Classify this cell by malaria status.
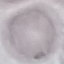
It is uninfected.

stain: Giemsa
image_type: automatically extracted cell patch, resized to 64 × 64 pixels
capture: smartphone through the microscope eyepiece
preparation: thin smear